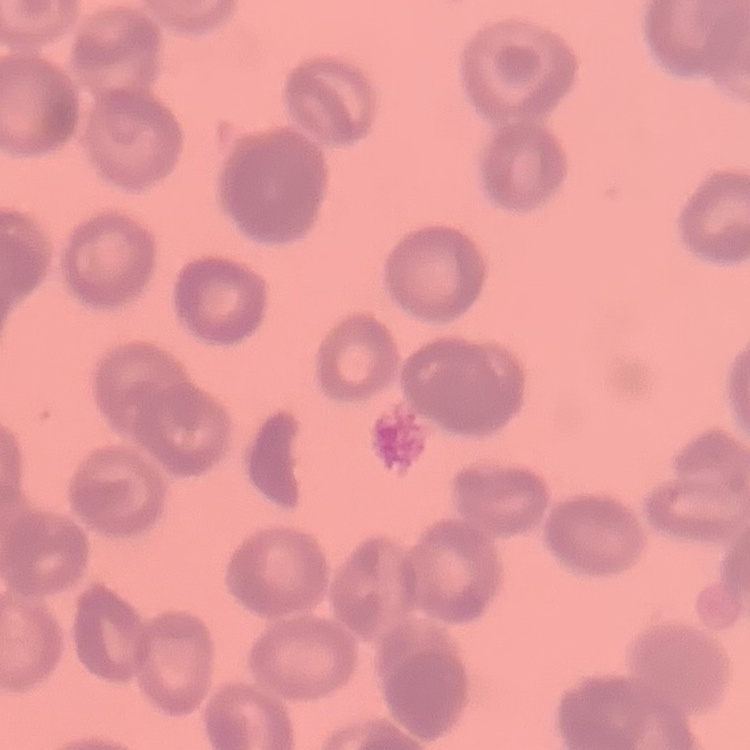 The red blood cells exhibit rouleaux formation. Field's or Giemsa stain. Square crop of a larger photomicrograph. Thin peripheral smear.